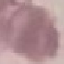
result = no malaria parasites seen
preparation = thin blood film
image type = automatically extracted cell patch, resized to 64 × 64 pixels
stain = Giemsa
capture = smartphone through the microscope eyepiece